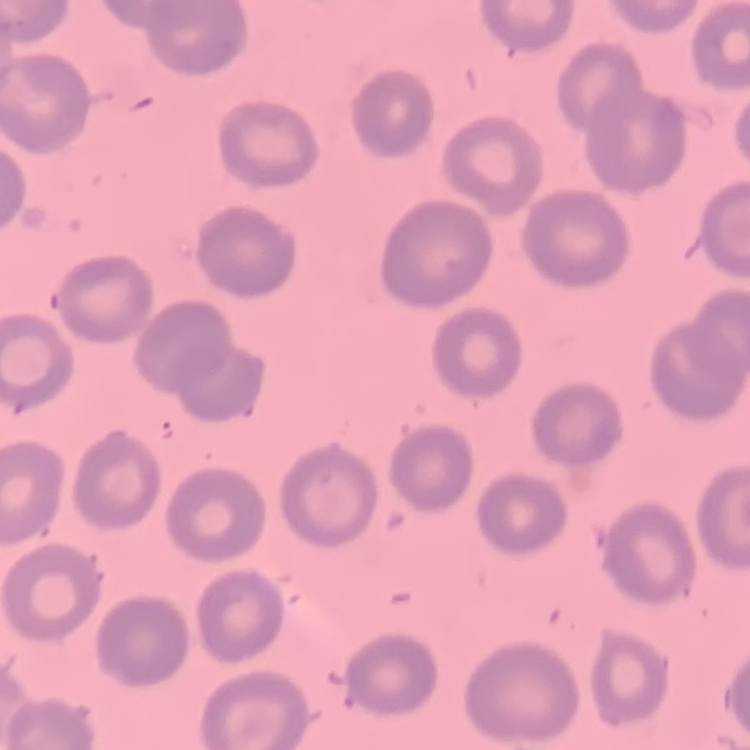 The red blood cells exhibit no rouleaux formation. Thin peripheral smear. One tile cut from a larger photomicrograph. Stained with either Field's or Giemsa.